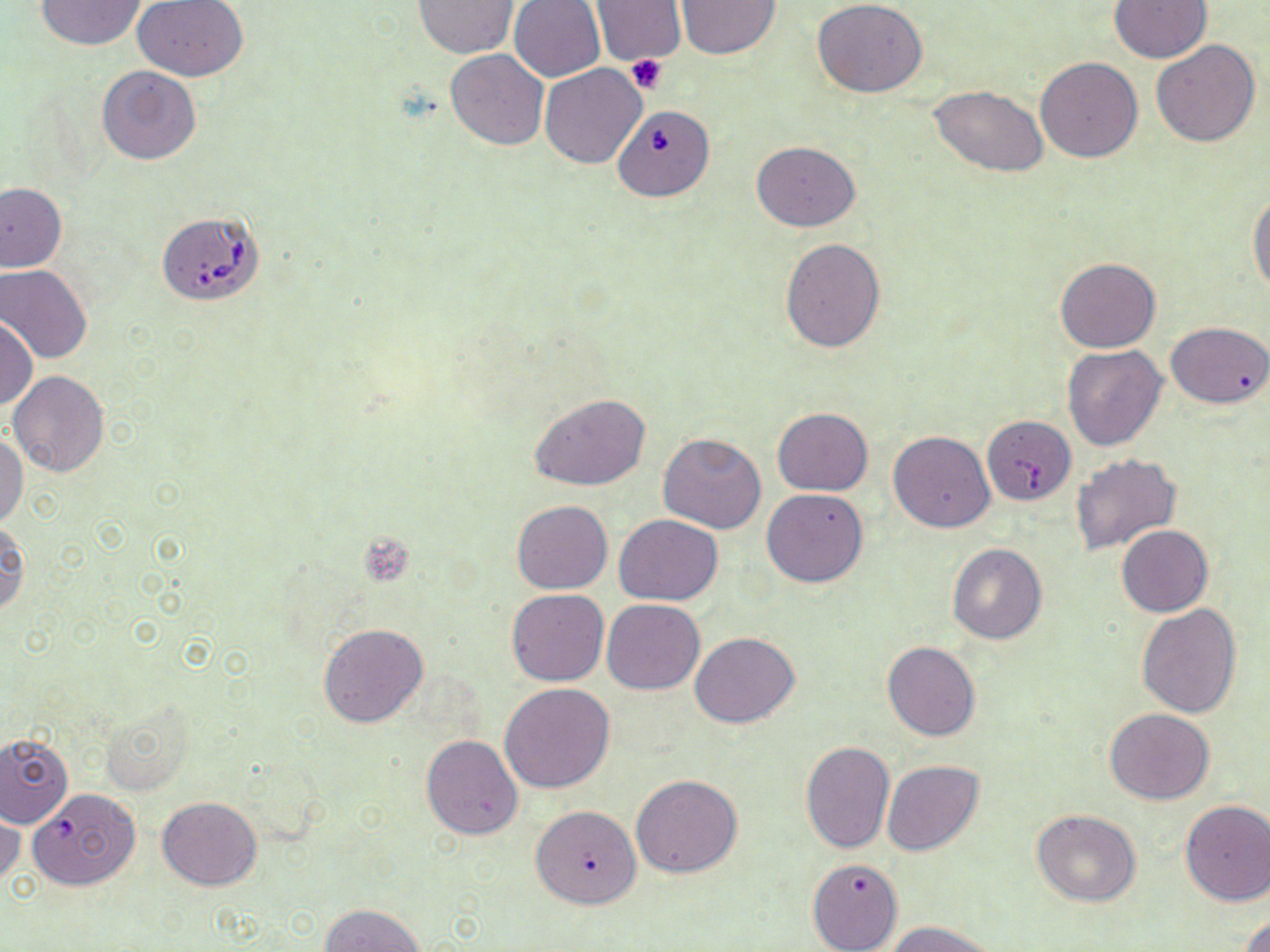

slide_level_diagnosis: Babesia divergens
preparation: thin blood film
uninfected_red_blood_cell_locations: 'approximate bounding boxes as [x1, y1, x2, y2] in pixels: [34, 0, 148, 51], [675, 0, 780, 59], [1110, 0, 1212, 64], [134, 1, 250, 82], [413, 1, 516, 58], [509, 1, 605, 83], [591, 1, 686, 65], [812, 1, 926, 98], [1152, 40, 1262, 147], [445, 49, 548, 150], [1035, 57, 1143, 161], [540, 64, 647, 168], [97, 66, 201, 165], [929, 84, 1051, 177], [751, 141, 860, 231], [0, 182, 67, 272], [1248, 192, 1270, 294], [779, 238, 886, 353], [1054, 256, 1161, 353], [0, 265, 93, 364], [0, 317, 38, 411], [1166, 321, 1270, 409], [1063, 344, 1167, 451], [7, 370, 110, 477], [529, 393, 652, 490], [772, 407, 872, 496], [982, 416, 1076, 504], [889, 430, 995, 533], [658, 432, 768, 534], [0, 433, 28, 530], [1070, 455, 1181, 556], [762, 488, 868, 587], [511, 500, 613, 593], [615, 514, 722, 605], [0, 517, 29, 619], [1116, 525, 1212, 617], [947, 544, 1047, 644], [506, 589, 609, 685], [601, 599, 706, 695], [1136, 603, 1243, 718], [318, 622, 427, 727], [690, 631, 799, 727], [883, 641, 981, 741], [500, 682, 616, 793], [1105, 708, 1216, 805], [0, 732, 73, 828], [421, 734, 523, 840], [800, 741, 895, 854], [881, 760, 984, 856], [631, 774, 742, 878], [28, 788, 140, 892], [157, 796, 261, 891], [1179, 801, 1270, 906], [0, 803, 22, 892], [531, 804, 641, 909], [1033, 810, 1141, 907], [808, 856, 903, 952], [320, 903, 423, 952], [1241, 910, 1269, 952], [886, 920, 997, 952]'
modality: light microscopy
image_size: 1270×952 pixels
babesia_divergens_infected_red_blood_cell_locations: 'approximate bounding boxes as [x1, y1, x2, y2] in pixels: [613, 104, 715, 204], [156, 210, 264, 306]'
platelet_locations: 'approximate bounding boxes as [x1, y1, x2, y2] in pixels: [625, 55, 667, 95]'
magnification: 1000x
field_of_view: one of a larger specimen
stain: May-Grünwald-Giemsa